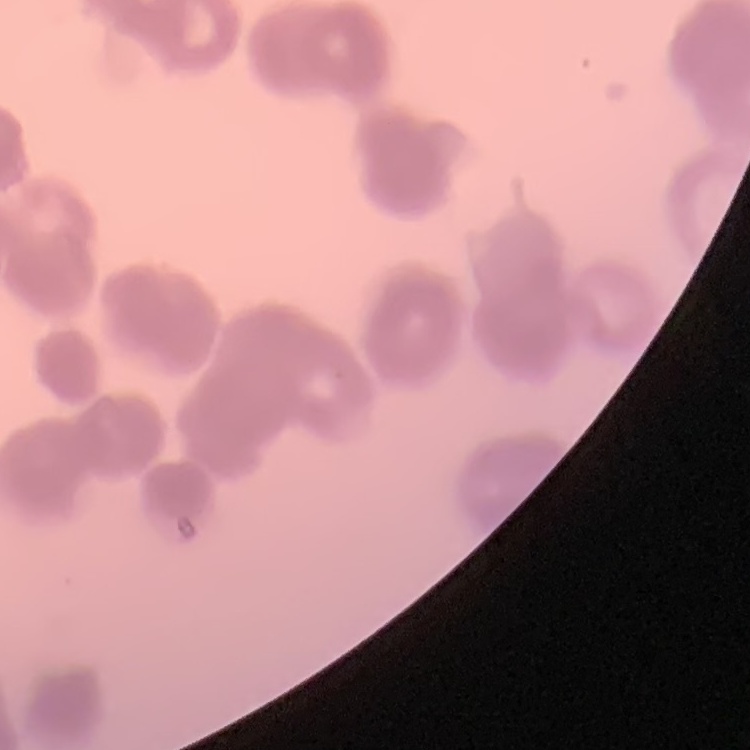

The red blood cells show rouleaux formation. Thin blood smear. Square crop of a larger photomicrograph. Stained with either Field's or Giemsa.